Assess this cell for malaria.
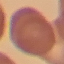
Uninfected.

Thin blood film. Acquired by smartphone through the microscope eyepiece. Giemsa-stained preparation. Cell patch, automatically extracted from a larger field of view and resized to 64 × 64 pixels.